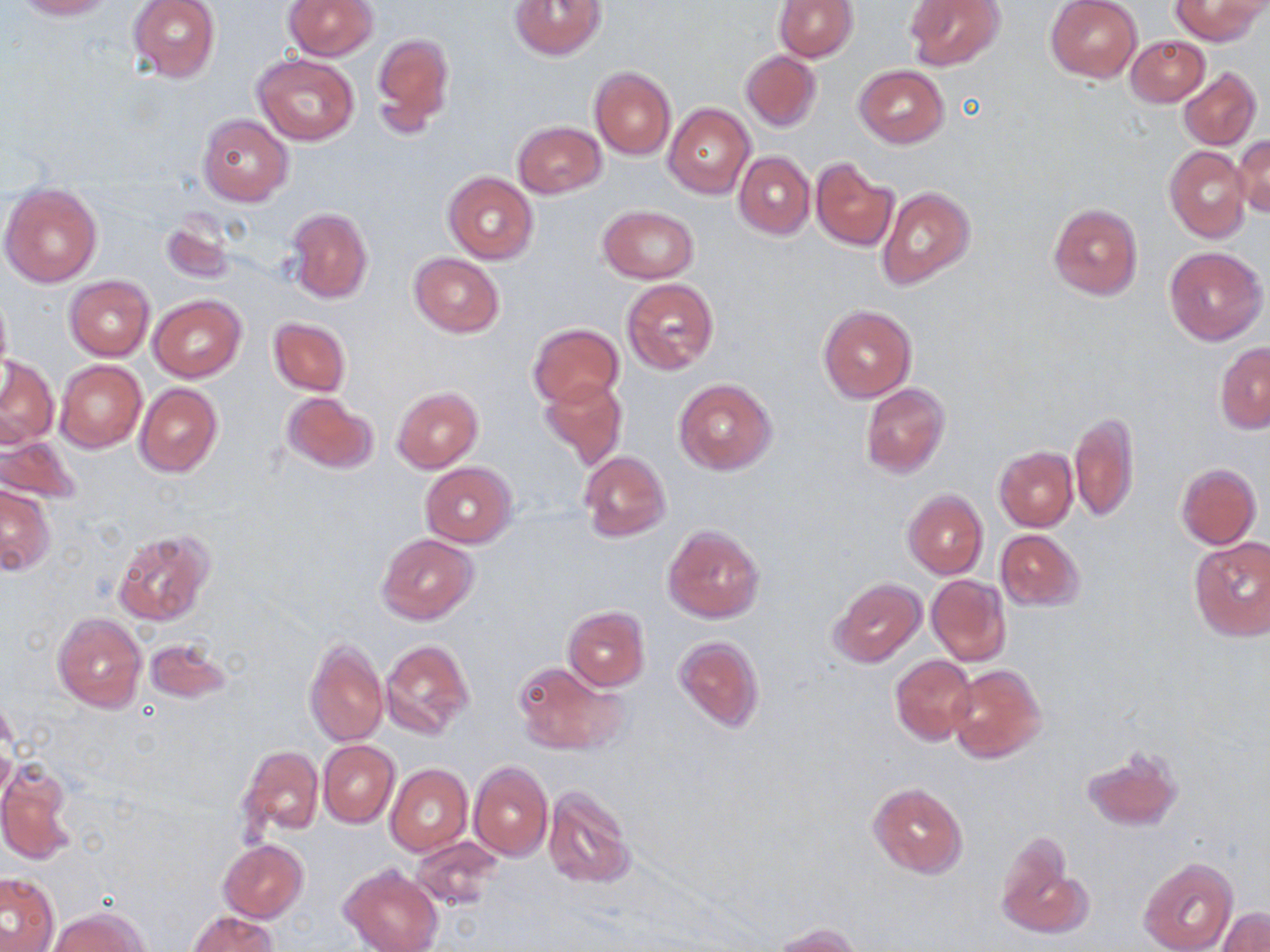
Summary:
  - Coordinate format: approximate bounding boxes as named x1/y1/x2/y2 corners in pixels
  - Uninfected red blood cell locations: (x1=12, y1=0, x2=114, y2=20), (x1=128, y1=0, x2=221, y2=83), (x1=284, y1=0, x2=378, y2=60), (x1=1045, y1=0, x2=1141, y2=83), (x1=1170, y1=0, x2=1265, y2=45), (x1=510, y1=1, x2=606, y2=60), (x1=774, y1=1, x2=857, y2=62), (x1=905, y1=1, x2=1004, y2=71), (x1=373, y1=32, x2=454, y2=137), (x1=1127, y1=34, x2=1210, y2=107), (x1=740, y1=51, x2=822, y2=132), (x1=253, y1=54, x2=359, y2=145), (x1=854, y1=65, x2=948, y2=148), (x1=1179, y1=67, x2=1260, y2=150), (x1=590, y1=68, x2=675, y2=159), (x1=664, y1=104, x2=754, y2=198), (x1=198, y1=114, x2=294, y2=207), (x1=512, y1=121, x2=606, y2=197), (x1=1232, y1=135, x2=1269, y2=216), (x1=1165, y1=146, x2=1249, y2=243), (x1=734, y1=151, x2=814, y2=239), (x1=811, y1=160, x2=897, y2=251), (x1=442, y1=171, x2=539, y2=264), (x1=1, y1=182, x2=102, y2=288), (x1=877, y1=186, x2=976, y2=291), (x1=1048, y1=204, x2=1143, y2=299), (x1=598, y1=206, x2=697, y2=283), (x1=287, y1=207, x2=373, y2=303), (x1=159, y1=215, x2=237, y2=285), (x1=1163, y1=245, x2=1267, y2=346), (x1=409, y1=252, x2=504, y2=337), (x1=64, y1=276, x2=154, y2=359), (x1=622, y1=278, x2=720, y2=376), (x1=0, y1=288, x2=12, y2=381), (x1=148, y1=295, x2=246, y2=383), (x1=818, y1=305, x2=916, y2=403), (x1=268, y1=317, x2=351, y2=396), (x1=529, y1=323, x2=624, y2=408), (x1=1215, y1=342, x2=1270, y2=432), (x1=0, y1=355, x2=58, y2=448), (x1=55, y1=360, x2=146, y2=453), (x1=0, y1=371, x2=67, y2=514), (x1=539, y1=376, x2=628, y2=467), (x1=673, y1=377, x2=778, y2=476), (x1=860, y1=383, x2=950, y2=478), (x1=134, y1=384, x2=222, y2=479), (x1=392, y1=386, x2=483, y2=473), (x1=280, y1=390, x2=379, y2=476), (x1=1070, y1=411, x2=1141, y2=524), (x1=0, y1=434, x2=83, y2=506), (x1=994, y1=447, x2=1077, y2=531), (x1=578, y1=451, x2=669, y2=542), (x1=420, y1=462, x2=518, y2=546), (x1=1176, y1=464, x2=1261, y2=549), (x1=0, y1=485, x2=55, y2=575), (x1=902, y1=489, x2=988, y2=579), (x1=662, y1=524, x2=764, y2=622), (x1=112, y1=529, x2=215, y2=629), (x1=995, y1=529, x2=1084, y2=611), (x1=376, y1=533, x2=478, y2=625), (x1=1187, y1=536, x2=1270, y2=642), (x1=927, y1=575, x2=1011, y2=666), (x1=828, y1=577, x2=927, y2=667), (x1=562, y1=605, x2=650, y2=691), (x1=52, y1=613, x2=147, y2=713), (x1=673, y1=635, x2=765, y2=733), (x1=305, y1=636, x2=388, y2=748), (x1=145, y1=637, x2=231, y2=703), (x1=380, y1=640, x2=473, y2=739), (x1=890, y1=654, x2=977, y2=745), (x1=511, y1=659, x2=624, y2=756), (x1=946, y1=664, x2=1046, y2=763), (x1=318, y1=741, x2=399, y2=827), (x1=1083, y1=745, x2=1183, y2=831), (x1=238, y1=746, x2=323, y2=840), (x1=470, y1=761, x2=553, y2=860), (x1=0, y1=763, x2=76, y2=866), (x1=386, y1=764, x2=472, y2=855), (x1=867, y1=782, x2=968, y2=878), (x1=541, y1=785, x2=635, y2=890), (x1=412, y1=836, x2=502, y2=910), (x1=996, y1=836, x2=1085, y2=940), (x1=219, y1=839, x2=309, y2=923), (x1=1139, y1=857, x2=1238, y2=952), (x1=339, y1=863, x2=442, y2=952), (x1=0, y1=874, x2=59, y2=950), (x1=49, y1=908, x2=149, y2=952), (x1=1218, y1=908, x2=1270, y2=952), (x1=187, y1=912, x2=279, y2=952), (x1=771, y1=922, x2=864, y2=951)
  - Slide-level diagnosis: no evidence of blood parasites
  - Image size: 1270×952 pixels
  - Field of view: one of a larger specimen
  - Stain: May-Grünwald-Giemsa
  - Magnification: 1000x
  - Modality: light microscopy
  - Preparation: thin blood film